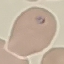 Malaria status: parasitized. Thin smear of blood. Giemsa-stained preparation. Cell patch, automatically extracted from a larger field of view and resized to 64 × 64 pixels. Photographed with a smartphone camera at the microscope eyepiece.